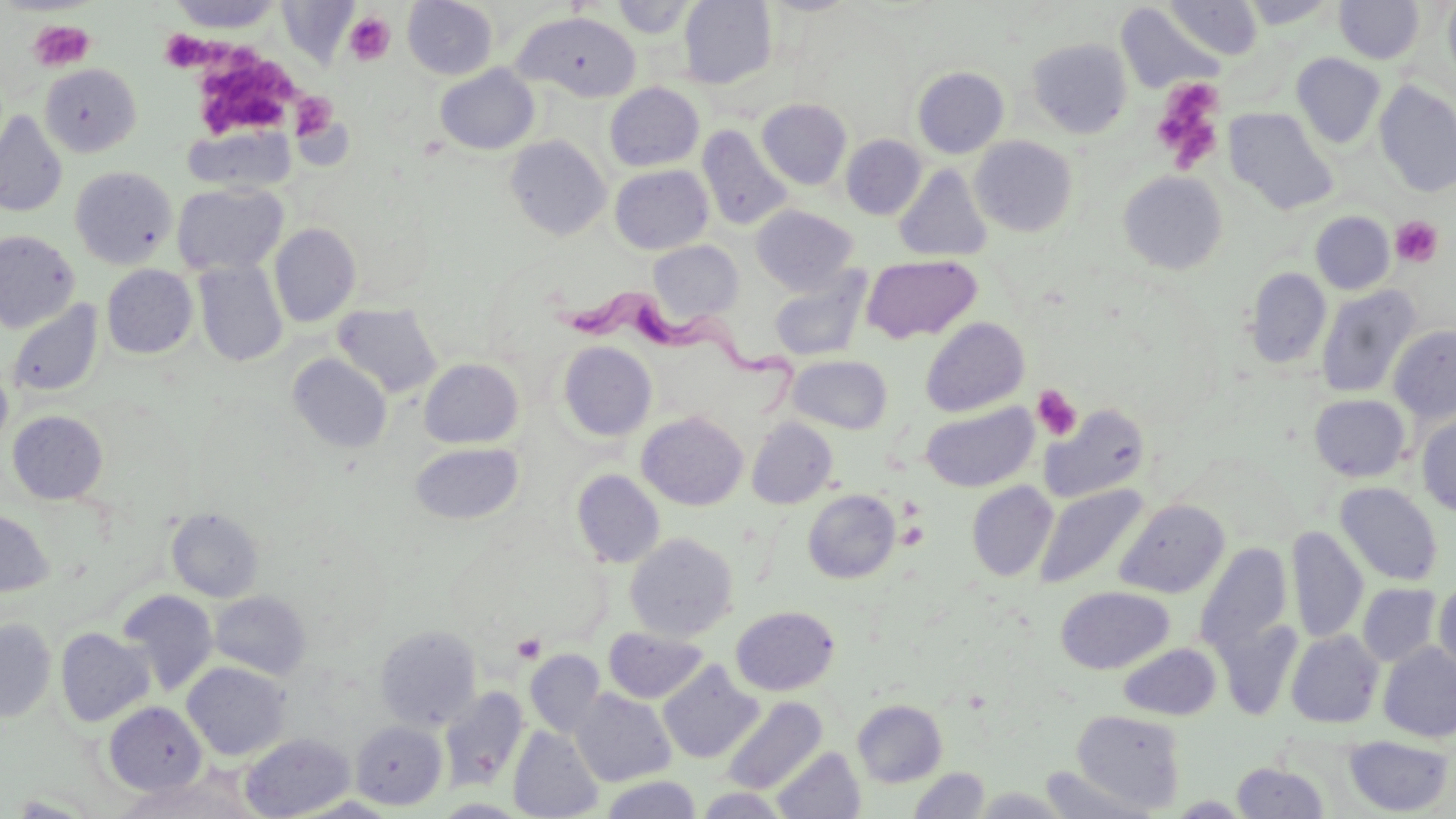

Summary:
  - Coordinate format: approximate bounding boxes as [x1, y1, x2, y2] in pixels
  - Platelet locations: [344, 12, 395, 64], [28, 19, 96, 71], [158, 29, 214, 71], [204, 46, 284, 132], [1151, 83, 1223, 171], [289, 92, 337, 139], [1391, 217, 1444, 267], [1031, 384, 1082, 440], [897, 520, 929, 548], [513, 634, 545, 663]
  - Uninfected red blood cell locations: [167, 0, 284, 32], [402, 0, 498, 79], [610, 0, 699, 38], [678, 0, 778, 88], [1165, 0, 1260, 60], [1240, 0, 1336, 29], [1334, 0, 1424, 64], [1443, 0, 1456, 87], [278, 1, 359, 66], [1116, 4, 1221, 92], [513, 11, 642, 102], [1027, 38, 1132, 138], [1292, 53, 1385, 148], [40, 64, 142, 157], [435, 64, 539, 155], [912, 67, 1009, 158], [1374, 80, 1456, 197], [605, 82, 704, 171], [757, 99, 852, 189], [1224, 108, 1338, 215], [0, 110, 67, 217], [184, 125, 293, 193], [697, 125, 792, 230], [504, 135, 611, 241], [841, 135, 927, 219], [970, 136, 1078, 237], [609, 164, 713, 254], [894, 164, 992, 263], [70, 165, 178, 269], [1118, 171, 1227, 274], [172, 183, 286, 276], [751, 205, 858, 294], [1311, 212, 1395, 295], [269, 223, 361, 327], [0, 230, 80, 333], [648, 240, 743, 324], [862, 255, 981, 343], [192, 261, 288, 366], [102, 264, 197, 358], [1245, 268, 1331, 369], [769, 270, 871, 362], [1316, 285, 1422, 399], [7, 301, 105, 398], [332, 303, 442, 398], [920, 317, 1029, 417], [1388, 324, 1456, 423], [558, 341, 657, 441], [287, 353, 392, 453], [787, 355, 892, 434], [419, 359, 523, 448], [0, 363, 13, 452], [1310, 394, 1410, 482], [921, 402, 1038, 491], [1040, 404, 1150, 503], [7, 410, 108, 504], [636, 411, 748, 510], [1416, 414, 1456, 517], [747, 418, 838, 509], [410, 442, 523, 525], [570, 469, 665, 568], [966, 481, 1057, 581], [1335, 482, 1443, 586], [1035, 484, 1150, 589], [803, 489, 901, 583], [1115, 499, 1229, 598], [167, 508, 264, 602], [0, 509, 54, 597], [1287, 526, 1367, 644], [624, 533, 738, 641], [1195, 542, 1293, 659], [1433, 581, 1456, 677], [1358, 583, 1441, 667], [1055, 586, 1174, 674], [117, 589, 219, 696], [209, 591, 311, 679], [730, 606, 839, 695], [0, 618, 57, 722], [1218, 621, 1300, 717], [375, 626, 481, 730], [55, 628, 154, 726], [603, 628, 709, 704], [1286, 630, 1383, 728], [1378, 642, 1456, 742], [1118, 643, 1220, 720], [525, 649, 605, 738], [657, 661, 763, 764], [182, 662, 291, 761], [439, 687, 528, 791], [571, 690, 676, 786], [722, 697, 826, 794], [852, 699, 947, 787], [104, 701, 207, 795], [1073, 709, 1186, 812], [351, 720, 447, 809], [508, 727, 603, 818], [239, 733, 355, 819], [1344, 735, 1453, 816], [771, 746, 866, 819], [1232, 761, 1329, 818], [1041, 766, 1157, 818], [908, 767, 990, 818], [114, 775, 258, 818], [601, 775, 701, 819], [695, 787, 791, 818], [970, 787, 1072, 818], [8, 794, 98, 818], [294, 796, 401, 818], [432, 799, 531, 818]
  - Trypanosoma brucei locations: [550, 287, 806, 420]
  - Slide-level diagnosis: Trypanosoma brucei
  - Modality: optical microscopy
  - Magnification: 1000x
  - Preparation: thin blood smear
  - Image size: 1456×819 pixels
  - Field of view: single
  - Stain: May-Grünwald-Giemsa